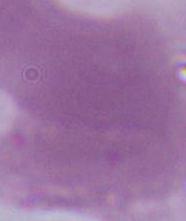
Summary:
  - Modality: micrograph
  - Identification: erythrocyte
  - Magnification: 1000x